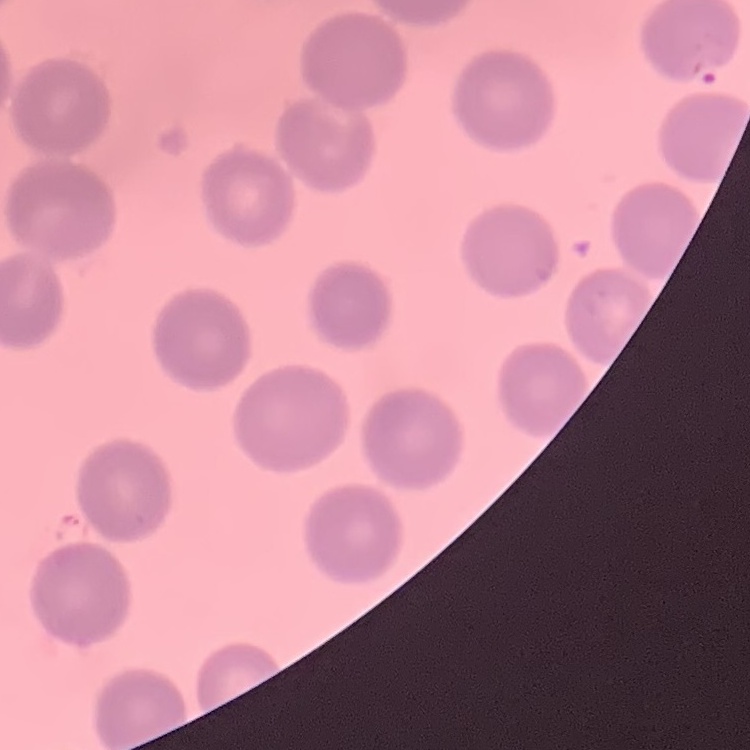
The red blood cells exhibit no rouleaux formation. One tile cut from a larger photomicrograph. Thin blood smear. Stained with either Field's or Giemsa.